Name the parasite shown.
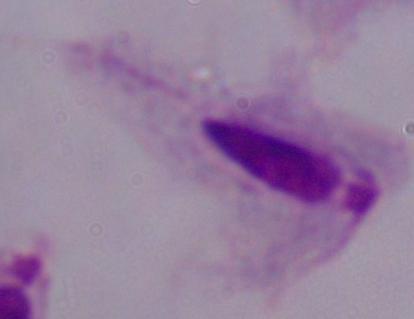
This is a trichomonad.

Summary:
  - Magnification: 1000x
  - Modality: micrograph